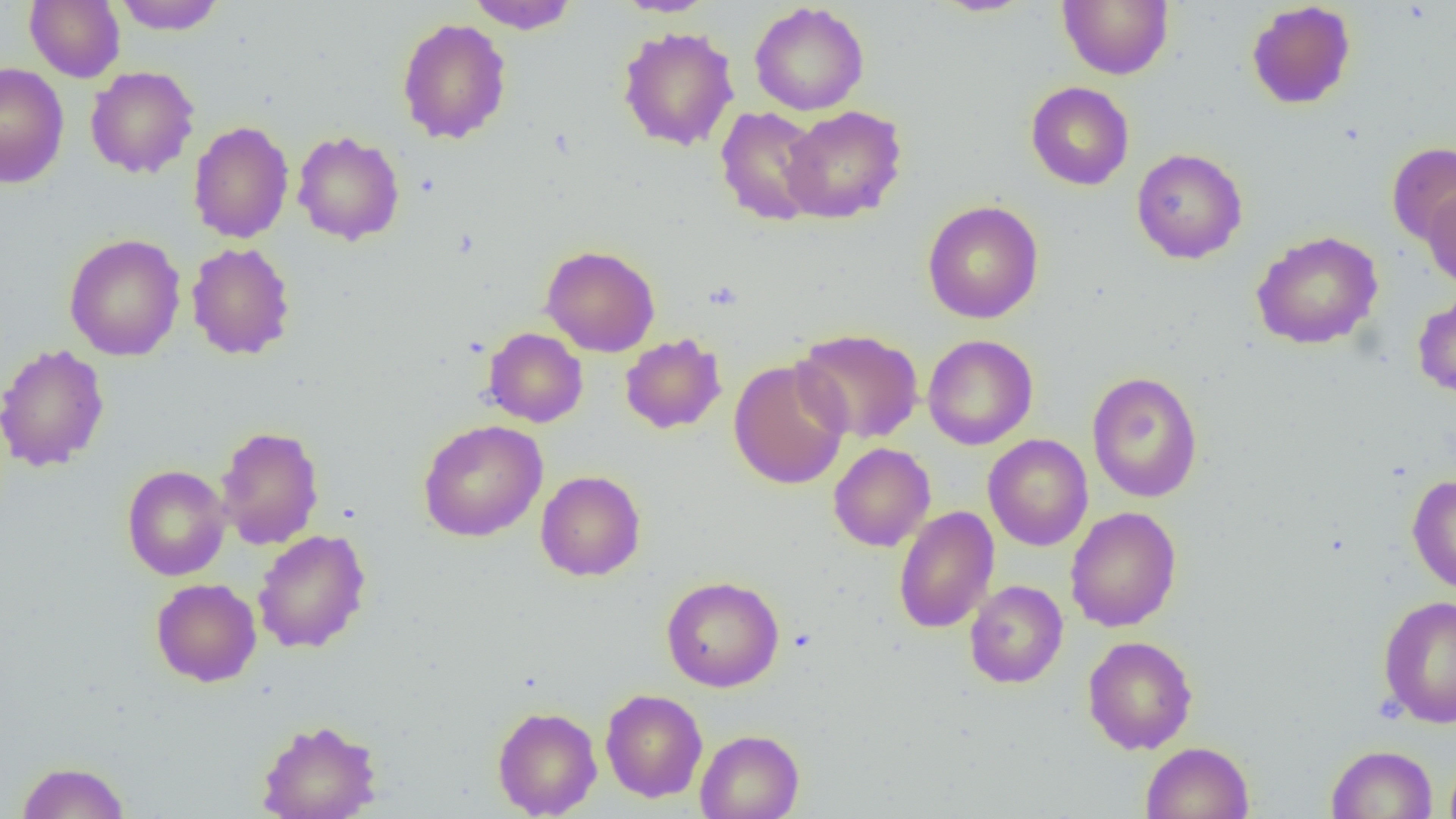
Summary:
  - Coordinate format: approximate bounding boxes as (x1, y1, x2, y2) in pixels
  - Uninfected red blood cell locations: (25, 0, 125, 83), (112, 0, 226, 35), (466, 0, 580, 33), (614, 0, 719, 17), (929, 0, 1038, 17), (1058, 0, 1173, 79), (1246, 1, 1357, 109), (749, 2, 870, 116), (396, 17, 512, 145), (617, 26, 739, 151), (0, 62, 69, 189), (85, 66, 199, 179), (1025, 81, 1134, 190), (781, 105, 907, 224), (715, 106, 827, 227), (188, 121, 294, 244), (292, 130, 405, 245), (1386, 141, 1456, 247), (1131, 148, 1248, 264), (1423, 186, 1456, 289), (922, 200, 1044, 324), (1250, 230, 1383, 350), (64, 233, 186, 361), (186, 242, 296, 360), (540, 244, 661, 357), (1413, 292, 1456, 398), (483, 327, 588, 427), (793, 328, 924, 444), (620, 333, 727, 434), (923, 334, 1038, 450), (0, 342, 110, 472), (728, 358, 852, 490), (1087, 371, 1203, 503), (418, 419, 547, 542), (214, 425, 325, 550), (983, 433, 1093, 551), (829, 442, 936, 552), (122, 464, 231, 581), (535, 470, 646, 581), (1407, 474, 1456, 595), (893, 506, 999, 633), (1066, 506, 1182, 632), (252, 529, 371, 654), (661, 575, 784, 692), (151, 578, 262, 687), (965, 580, 1068, 688), (1377, 595, 1456, 728), (1082, 635, 1198, 754), (600, 688, 708, 802), (492, 706, 602, 818), (256, 719, 382, 819), (695, 729, 805, 819), (1140, 741, 1253, 819), (1325, 745, 1438, 818), (1444, 749, 1456, 819), (16, 761, 130, 819)
  - Slide-level diagnosis: negative for blood parasites
  - Image size: 1456×819 pixels
  - Preparation: thin blood film
  - Field of view: one of a larger specimen
  - Modality: optical microscopy
  - Magnification: 1000x